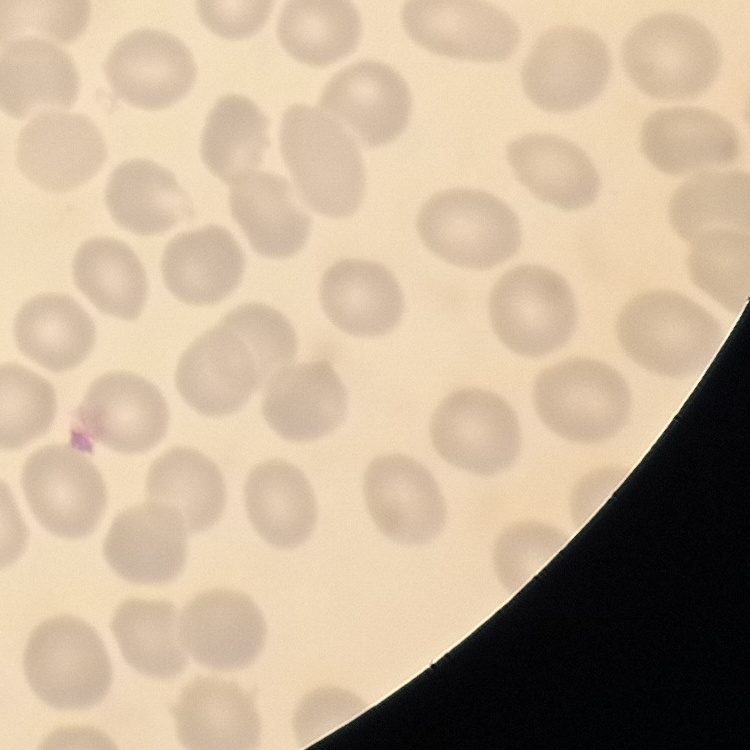
The red blood cells exhibit no rouleaux formation. One tile cut from a larger photomicrograph. Field's or Giemsa stain. Thin peripheral smear.